State which parasite is depicted.
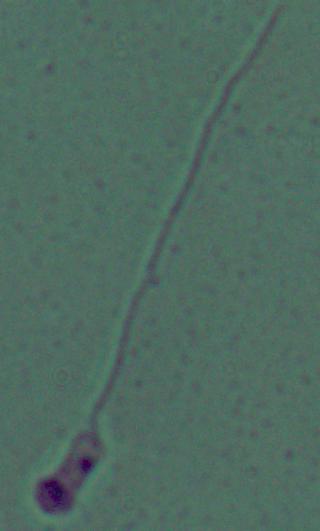
Leishmania.

Summary:
  - Modality: micrograph
  - Magnification: 1000x